Name the parasite shown.
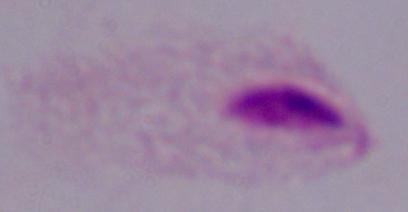
This is a trichomonad.

Summary:
  - Modality: micrograph
  - Magnification: 1000x